Assess this cell for malaria.
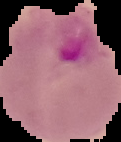

Parasitized.

The area outside the segmented cell region is set to black. From a thin blood film. Image is 121×142 pixels.